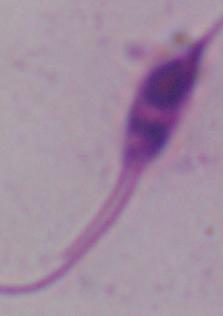

1000x magnification. A Leishmania parasite is shown. Photomicrograph.